Locate and identify every blood parasite.
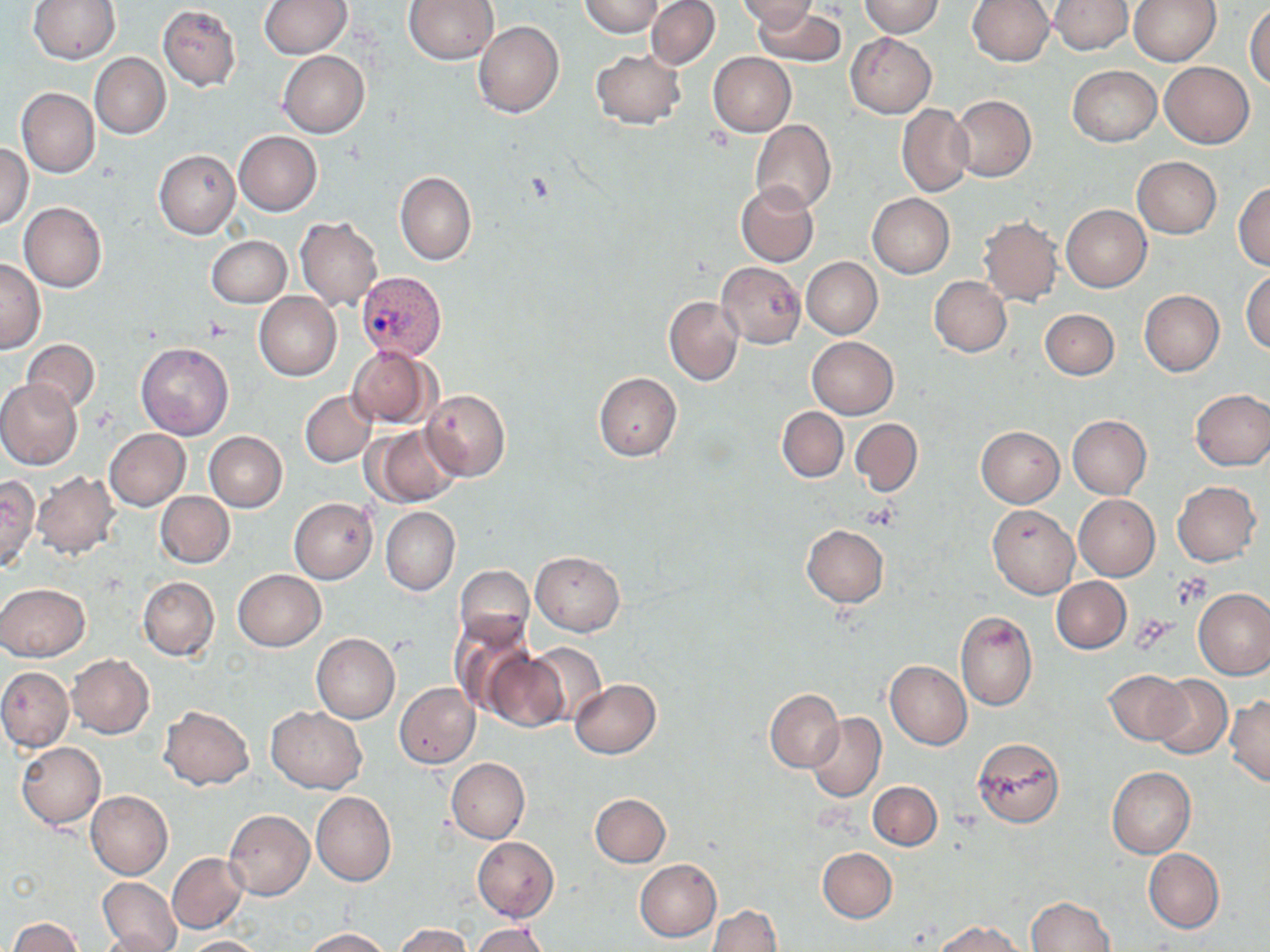

Approximate bounding boxes as (x1, y1, x2, y2) in pixels.
Plasmodium vivax-infected red blood cells: (356, 271, 447, 361).
No Plasmodium falciparum, Plasmodium ovale, Plasmodium malariae, Babesia divergens, or Trypanosoma brucei observed.

Platelet locations: (1135, 616, 1175, 648). Uninfected red blood cell locations: (28, 0, 121, 64), (404, 0, 499, 64), (577, 0, 663, 36), (646, 0, 720, 69), (736, 0, 817, 27), (1050, 0, 1131, 54), (1130, 0, 1221, 65), (258, 1, 350, 58), (860, 1, 944, 37), (966, 1, 1054, 67), (1246, 3, 1270, 89), (157, 4, 241, 92), (754, 5, 844, 68), (472, 19, 564, 118), (847, 33, 936, 118), (591, 50, 685, 130), (277, 51, 369, 138), (708, 52, 796, 135), (90, 53, 170, 140), (1160, 62, 1254, 148), (1068, 65, 1160, 147), (16, 87, 100, 177), (949, 95, 1036, 182), (897, 104, 973, 197), (751, 119, 835, 214), (233, 131, 322, 215), (0, 144, 33, 228), (154, 149, 240, 238), (1132, 156, 1222, 238), (395, 171, 477, 266), (736, 181, 819, 266), (1233, 181, 1270, 272), (867, 193, 954, 277), (19, 202, 107, 292), (1061, 205, 1151, 291), (978, 215, 1062, 305), (295, 216, 382, 310), (206, 236, 291, 306), (802, 258, 882, 338), (0, 259, 47, 353), (717, 261, 806, 349), (1242, 269, 1270, 354), (930, 276, 1012, 356), (1138, 290, 1224, 377), (254, 293, 342, 380), (664, 296, 743, 385), (1040, 309, 1119, 380), (807, 336, 899, 418), (22, 339, 100, 412), (135, 342, 233, 440), (346, 345, 436, 428), (593, 373, 682, 461), (0, 379, 82, 471), (421, 389, 510, 482), (1190, 389, 1270, 470), (300, 390, 376, 467), (777, 407, 848, 481), (1067, 416, 1151, 498), (851, 419, 922, 496), (366, 425, 463, 507), (976, 426, 1064, 507), (105, 428, 190, 510), (203, 431, 288, 511), (32, 471, 119, 558), (0, 475, 39, 571), (1171, 481, 1261, 567), (155, 492, 234, 568), (1073, 494, 1159, 579), (289, 497, 377, 582), (987, 504, 1079, 598), (381, 507, 459, 596), (802, 525, 889, 608), (531, 550, 624, 635), (455, 565, 534, 648), (233, 569, 327, 651), (138, 576, 219, 659), (1052, 577, 1131, 653), (0, 583, 90, 661), (1194, 588, 1270, 680), (956, 610, 1037, 712), (450, 616, 535, 717), (311, 633, 400, 723), (527, 643, 607, 725), (484, 652, 569, 732), (66, 654, 154, 738), (883, 660, 971, 749), (0, 667, 73, 752), (1104, 669, 1187, 745), (1150, 674, 1231, 759), (569, 679, 660, 758), (394, 683, 480, 769), (765, 689, 843, 772), (1226, 695, 1270, 785), (158, 705, 255, 789), (266, 706, 367, 793), (807, 712, 886, 802), (972, 738, 1066, 828), (15, 742, 105, 829), (446, 758, 529, 843), (1107, 767, 1195, 858), (868, 781, 941, 850), (86, 791, 173, 879), (311, 791, 395, 887), (590, 793, 670, 867), (224, 810, 314, 899), (473, 837, 559, 920), (817, 848, 897, 923), (1144, 849, 1224, 933), (167, 853, 248, 933), (635, 859, 721, 941), (101, 865, 248, 942), (97, 877, 181, 952), (1027, 897, 1115, 951), (707, 906, 782, 952), (7, 918, 83, 952), (935, 920, 1023, 952), (396, 924, 471, 951), (471, 924, 554, 952), (302, 928, 391, 951), (96, 929, 177, 952), (183, 936, 264, 952). Slide-level diagnosis: Plasmodium vivax. One field of a larger specimen. May-Grünwald-Giemsa-stained preparation. Image is 1270×952 pixels. Light microscopy. Thin blood smear. 1000x magnification.